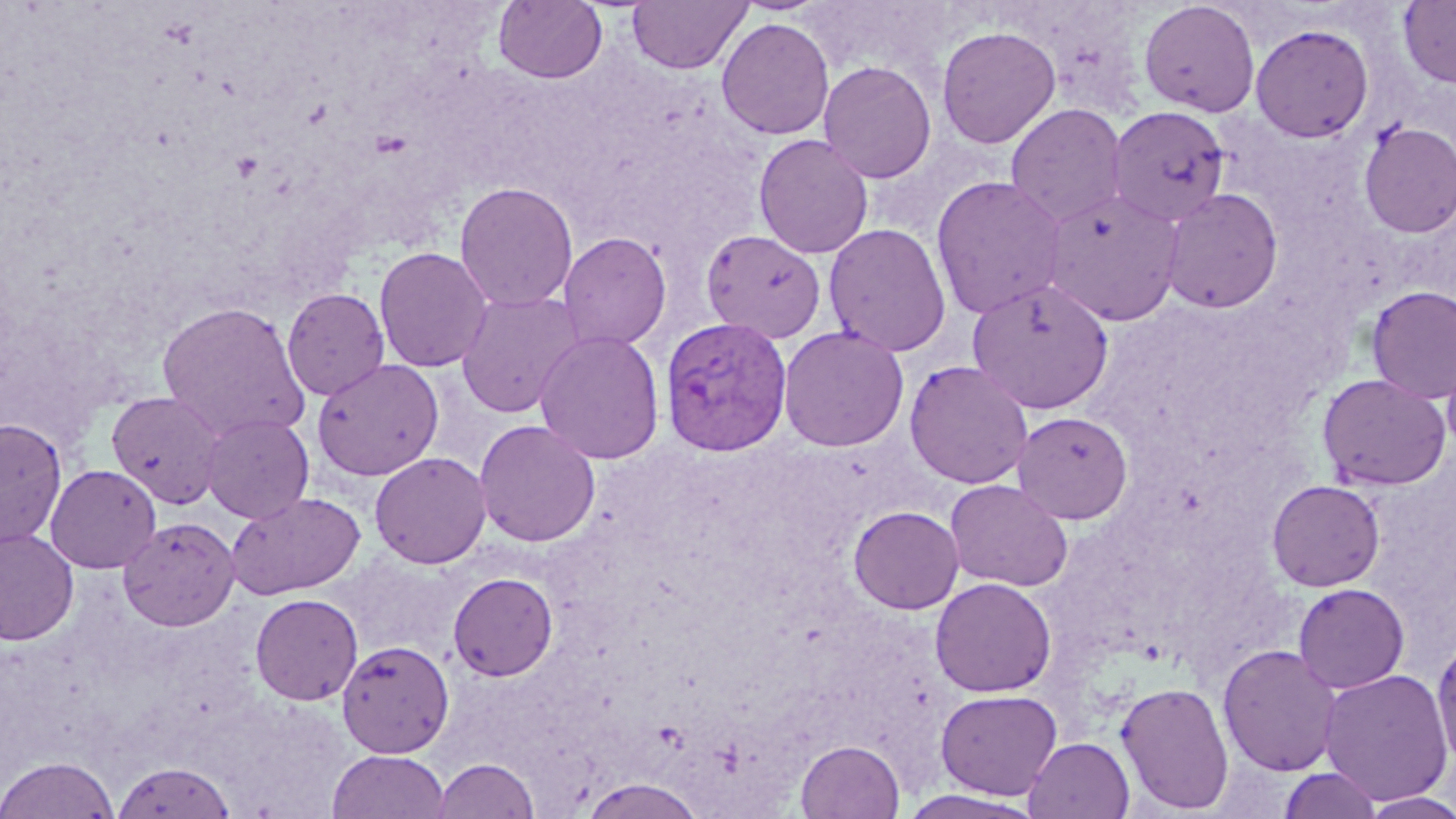
Summary:
  - Coordinate format: approximate bounding boxes as (x1,y1)-(x2,y2) corner pairs in pixels
  - Plasmodium vivax-infected red blood cell locations: (659,316)-(793,456)
  - Uninfected red blood cell locations: (493,0)-(608,84), (626,0)-(753,75), (1139,1)-(1261,117), (1398,1)-(1456,88), (716,17)-(835,139), (1250,23)-(1374,142), (937,25)-(1061,148), (818,61)-(937,183), (1006,103)-(1127,229), (1107,106)-(1230,227), (1359,121)-(1456,237), (753,133)-(874,258), (931,175)-(1067,320), (454,181)-(578,312), (1040,188)-(1182,326), (1160,188)-(1283,314), (823,223)-(952,357), (700,228)-(826,342), (558,232)-(672,352), (373,246)-(493,373), (966,278)-(1114,414), (1366,285)-(1456,403), (281,287)-(390,400), (455,289)-(586,419), (157,301)-(310,441), (777,325)-(909,453), (534,329)-(665,465), (1441,342)-(1456,459), (312,359)-(444,481), (904,360)-(1034,489), (1317,373)-(1451,491), (106,391)-(227,508), (1012,411)-(1133,524), (200,413)-(314,523), (0,418)-(67,548), (474,419)-(601,547), (370,451)-(491,569), (45,464)-(161,573), (944,479)-(1073,592), (1266,479)-(1385,591), (225,491)-(366,599), (848,506)-(964,614), (118,516)-(239,631), (0,528)-(79,645), (448,572)-(558,681), (930,577)-(1056,697), (1293,583)-(1410,693), (250,593)-(363,705), (1431,636)-(1456,771), (337,640)-(454,758), (1218,644)-(1342,776), (1319,668)-(1453,806), (1116,681)-(1234,814), (936,689)-(1062,800), (1024,737)-(1135,819), (795,739)-(905,818), (327,750)-(450,818), (1,756)-(118,818), (431,758)-(540,818), (112,760)-(236,819), (1279,767)-(1383,818), (577,776)-(708,818), (897,789)-(1047,818), (1359,791)-(1456,818)
  - Slide-level diagnosis: Plasmodium vivax
  - Preparation: thin blood smear
  - Field of view: one of a larger specimen
  - Magnification: 1000x
  - Modality: light microscopy
  - Stain: May-Grünwald-Giemsa
  - Image size: 1456×819 pixels